Report the malaria status of this cell.
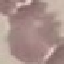
Uninfected.

Thin blood smear. Giemsa-stained preparation. Photographed with a smartphone camera at the microscope eyepiece. Automatically extracted cell patch, resized to 64 × 64 pixels.